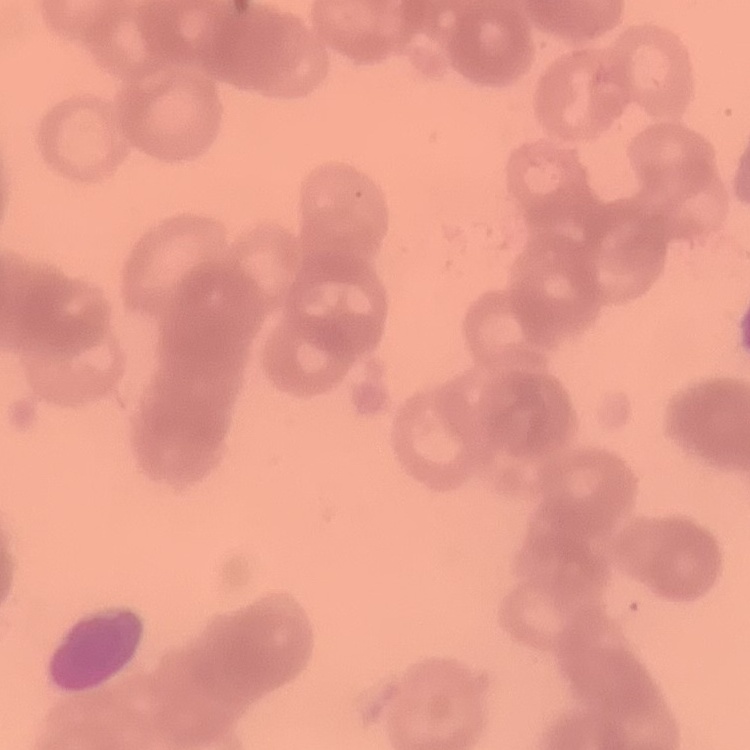 The erythrocytes exhibit rouleaux formation. Square crop of a larger photomicrograph. Thin peripheral smear. Stained with either Field's or Giemsa.